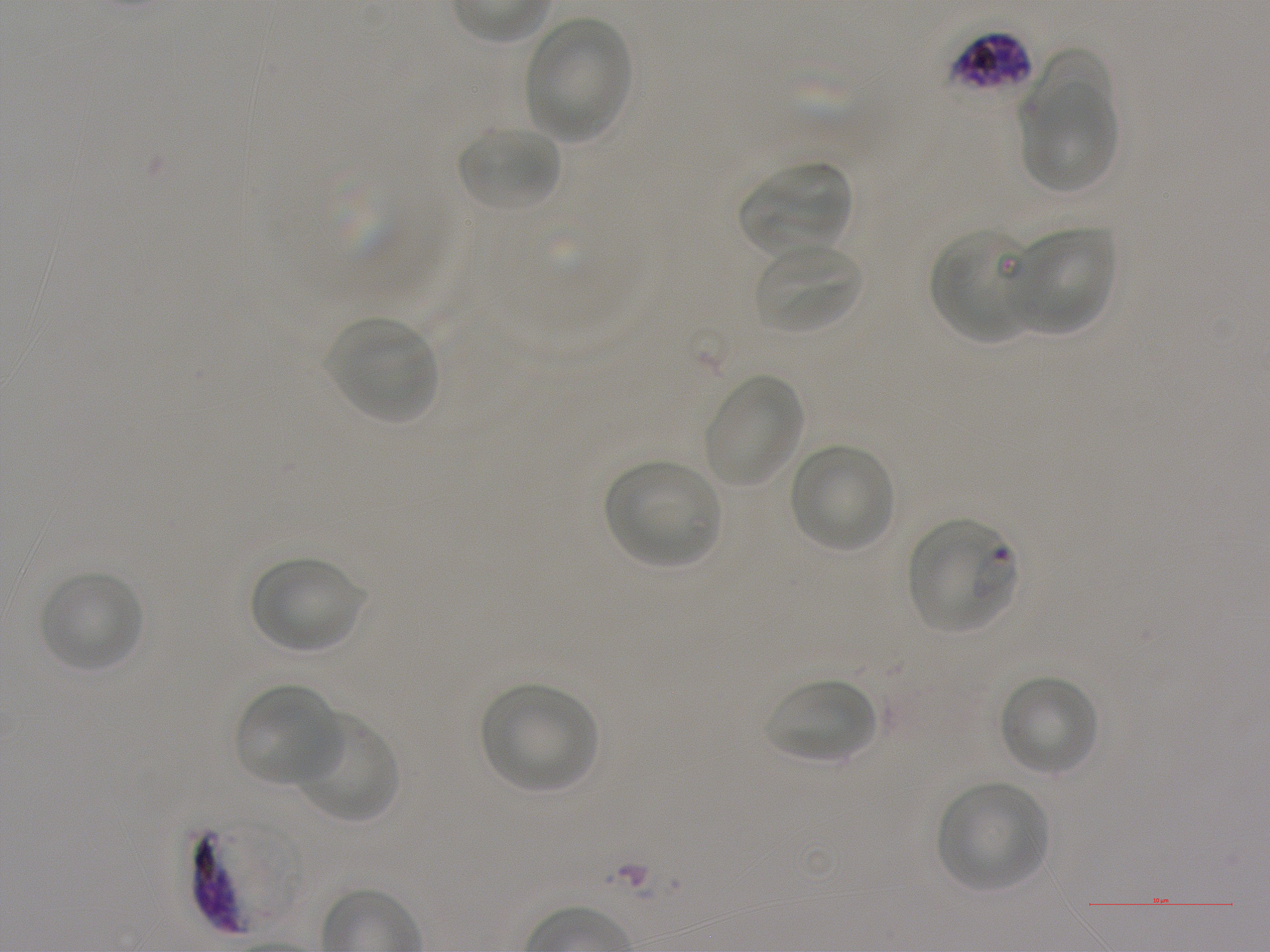

Approximate bounding boxes as [x1, y1, x2, y2] in pixels. Not every red blood cell is marked. A life-cycle stage — or a range of stages, where the recorded stages span more than one — follows each staged infected red blood cell.
Summary:
  - Locations of uninfected red blood cells: [524, 17, 632, 141], [1025, 47, 1113, 139], [1022, 82, 1118, 194], [456, 124, 562, 212], [740, 160, 853, 255], [1010, 226, 1116, 335], [930, 228, 1033, 342], [756, 243, 864, 335], [329, 317, 437, 424], [704, 375, 804, 487], [789, 444, 895, 553], [604, 458, 722, 568], [251, 556, 363, 654], [39, 570, 143, 673], [998, 674, 1099, 776], [765, 677, 876, 763], [235, 683, 340, 786], [480, 683, 597, 791], [292, 711, 400, 823], [937, 782, 1048, 891]
  - Locations of red blood cells of indeterminate infection status: [949, 31, 1031, 93]
  - Locations of infected red blood cells: [912, 523, 1017, 634] ring; [194, 817, 305, 934]
  - Image size: 1270×952 pixels
  - Preparation: thin blood film
  - Stain: Giemsa
  - Objective: 100x, oil immersion, numerical aperture 1.25
  - Field of view: one from this slide
  - Donor blood group: A+
  - Culture: in-vitro Plasmodium falciparum strain NF54, static